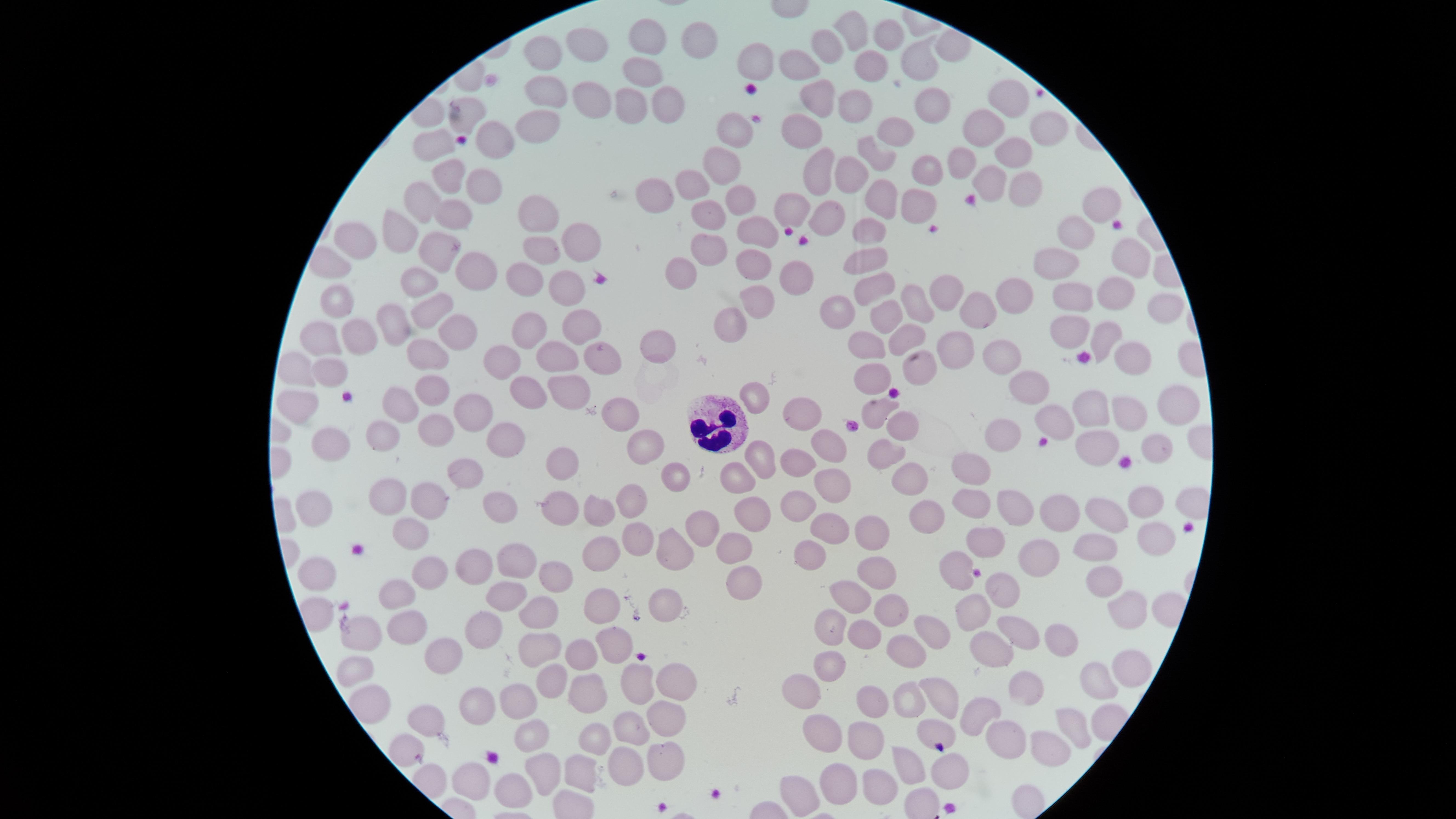

image size = 1456×819 pixels
visible region = circular
uninfected red blood cells = approximate marker points as (x, y) in pixels: (855, 26), (648, 30), (886, 32), (700, 39), (585, 41), (831, 44), (542, 57), (866, 59), (757, 60), (799, 64), (919, 64), (637, 72), (546, 95), (813, 95), (588, 97), (1004, 98), (667, 100), (929, 100), (848, 101), (622, 108), (465, 116), (532, 127), (981, 127), (798, 128), (894, 130), (1046, 130), (732, 132), (495, 134), (433, 136), (1007, 156), (882, 158), (958, 158), (723, 163), (819, 168), (447, 171), (847, 172), (922, 172), (986, 183), (696, 185), (478, 187), (662, 188), (1011, 189), (878, 195), (728, 196), (916, 199), (792, 201), (424, 203), (1093, 205), (454, 214), (704, 215), (825, 215), (537, 218), (752, 223), (871, 227), (1070, 229), (403, 233), (578, 238), (352, 244), (716, 244), (541, 251), (436, 253), (750, 256), (1134, 256), (864, 258), (1056, 258), (333, 263), (684, 264), (477, 266), (790, 273), (872, 277), (528, 280), (419, 281), (949, 289), (570, 290), (1017, 290), (1113, 291), (1075, 294), (335, 301), (757, 302), (916, 303), (1162, 307), (834, 309), (427, 310), (982, 310), (885, 314), (397, 321), (454, 324), (733, 325), (1074, 326), (358, 329), (530, 329), (904, 329), (577, 330), (1105, 332), (328, 333), (864, 342), (650, 347), (950, 347), (597, 350), (424, 352), (555, 355), (1129, 355), (995, 356), (497, 358), (915, 370), (295, 372), (330, 372), (874, 373), (430, 380), (1029, 385), (526, 389), (575, 391), (760, 397), (399, 400), (1177, 403), (296, 406), (1091, 407), (621, 408), (805, 409), (874, 410), (1129, 412), (473, 414), (892, 419), (1058, 422), (431, 424), (384, 429), (1002, 434), (508, 440), (821, 440), (333, 441), (637, 441), (1164, 446), (1085, 448), (884, 452), (760, 457), (796, 459), (564, 464), (466, 470), (983, 471), (667, 475), (734, 477), (910, 478), (838, 484), (395, 489), (430, 495), (634, 497), (320, 504), (503, 504), (966, 504), (804, 505), (1145, 506), (560, 508), (591, 509), (753, 510), (1020, 510), (1064, 512), (1106, 514), (920, 516), (829, 522), (704, 523), (406, 529), (635, 531), (870, 532), (984, 536), (1153, 536), (734, 539), (671, 546), (1042, 552), (518, 554), (814, 554), (1089, 554), (596, 557), (955, 565), (474, 566), (554, 572), (427, 573), (324, 575), (874, 575), (1099, 580), (736, 588), (1004, 588), (509, 592), (398, 594), (853, 596), (666, 602), (539, 603), (888, 603), (1115, 607), (597, 609), (974, 613), (404, 626), (835, 631), (868, 632), (480, 635), (1024, 636), (932, 637), (1065, 637), (364, 640), (611, 641), (900, 643), (982, 647), (431, 650), (584, 651), (537, 654), (1130, 658), (833, 665), (359, 672), (632, 680), (1096, 681), (548, 682), (668, 683), (801, 683), (1030, 687), (590, 689), (860, 690), (934, 693), (517, 697), (477, 700), (900, 700), (663, 716), (969, 717), (428, 718), (929, 724), (1079, 725), (633, 726), (527, 733), (822, 735), (595, 738), (400, 747), (863, 747), (1011, 747), (1053, 748), (663, 754), (626, 762), (913, 767), (948, 767), (581, 772), (464, 774), (545, 775), (507, 782), (834, 787), (793, 792), (881, 792)
field of view = single
preparation = thin blood smear
capture = smartphone photograph through the microscope eyepiece
presence = no malaria parasites detected
stain = Giemsa
white blood cells = approximate marker points as (x, y) in pixels: (712, 418)